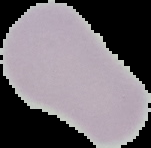

result = no malaria parasites seen
preparation = thin blood smear
image size = 151×148 pixels
image type = segmented cell region with the area outside set to black